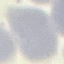

Result: negative for malaria parasites. Giemsa stain. Thin blood film. Cell patch, automatically extracted from a larger field of view and resized to 64 × 64 pixels. Photographed with a smartphone camera at the microscope eyepiece.